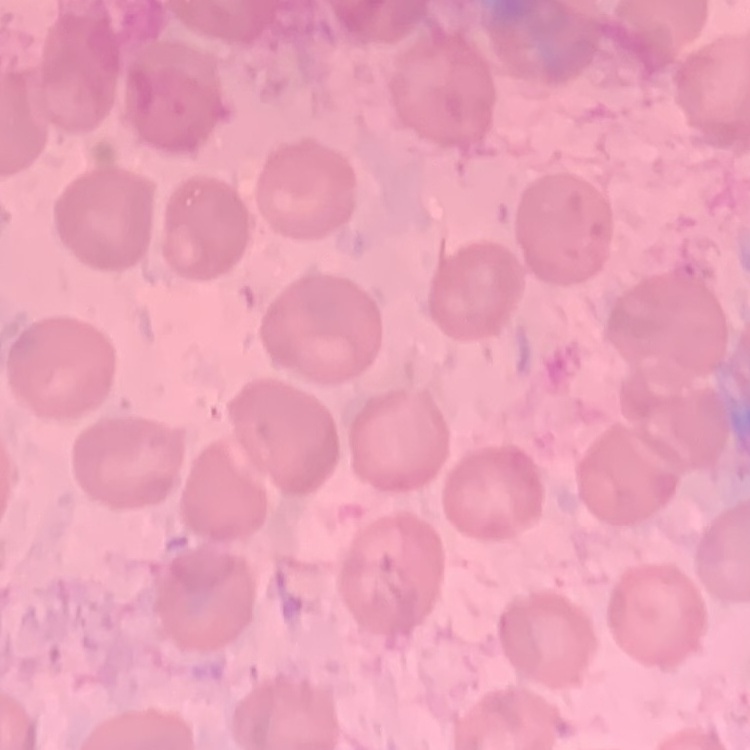

Summary:
  - Erythrocyte morphology: no rouleaux formation
  - Stain: Field's or Giemsa
  - Preparation: thin blood smear
  - Image type: square crop of a larger photomicrograph